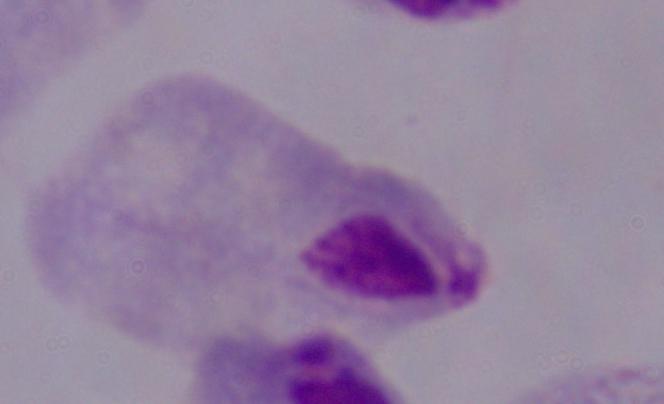
Photomicrograph. 1000x magnification. A trichomonad is seen.